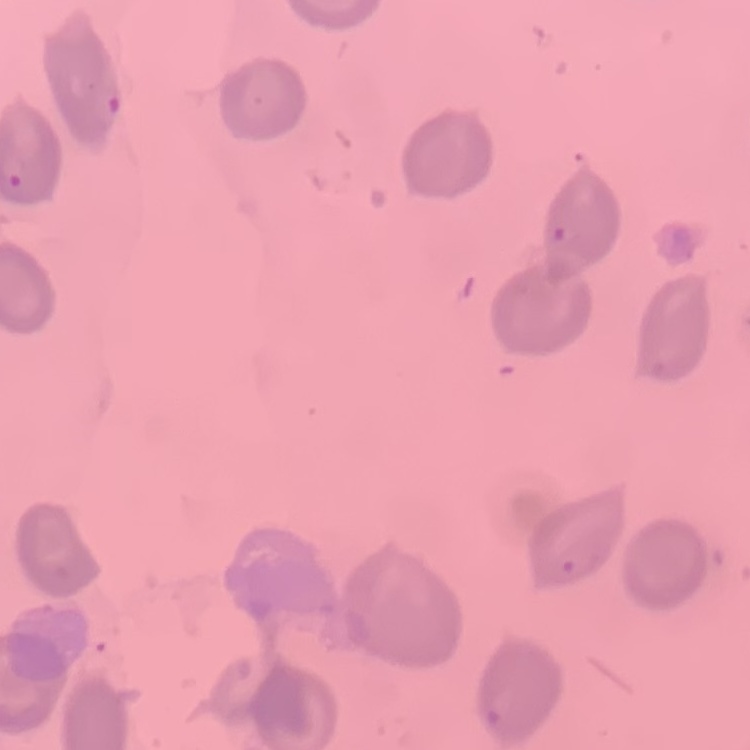

Summary:
  - Red blood cell morphology: no rouleaux formation
  - Preparation: thin blood film
  - Image type: square crop of a larger photomicrograph
  - Stain: Field's or Giemsa